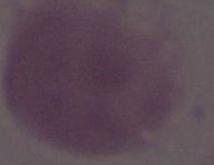
1000x magnification. Micrograph. A red blood cell is shown.